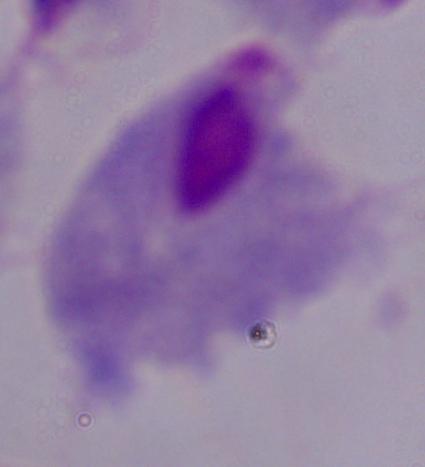
Summary:
  - Modality: photomicrograph
  - Magnification: 1000x
  - Identification: trichomonad